Identify the blood parasite species.
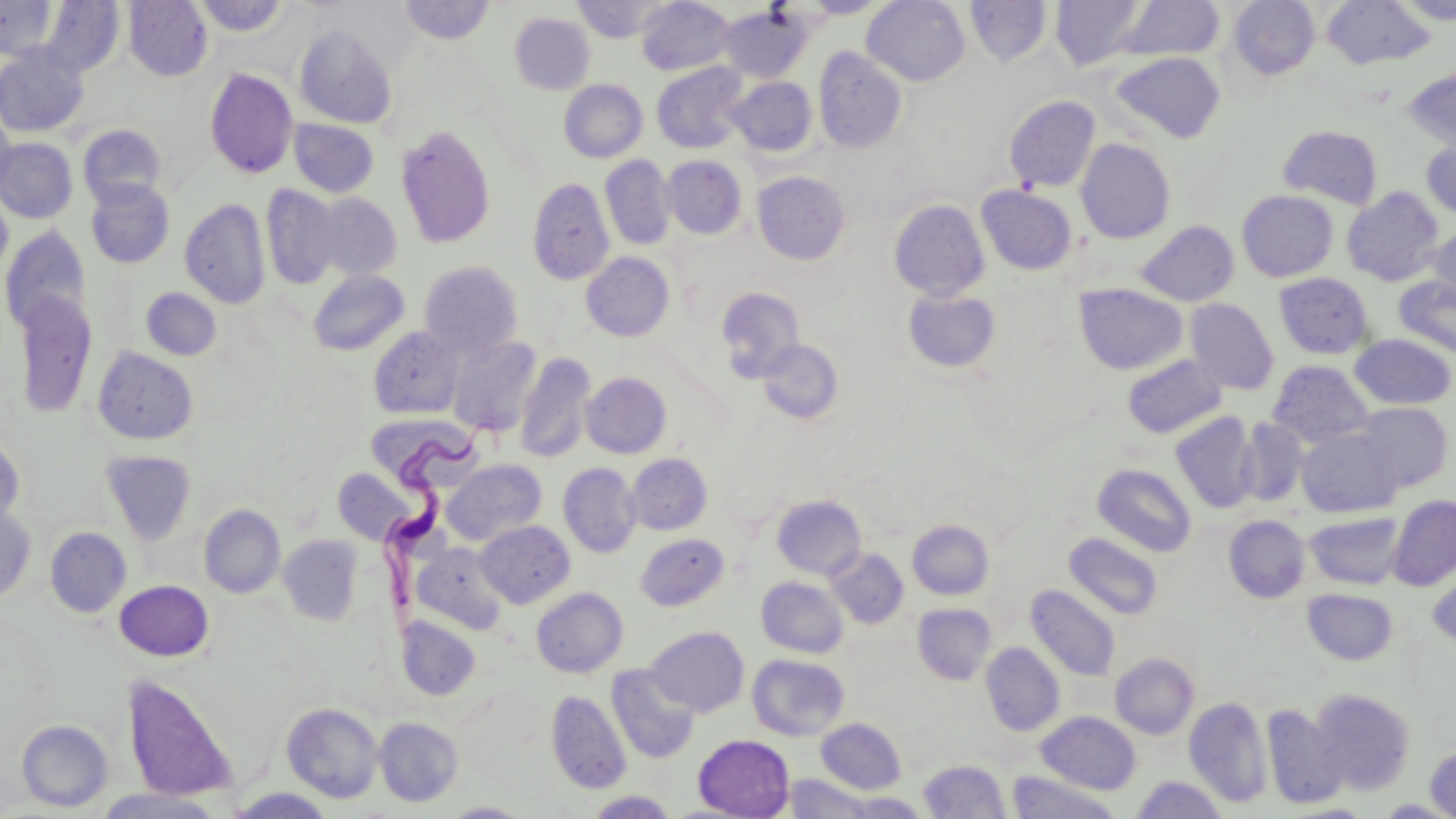

Trypanosoma brucei.

Summary:
  - Coordinate format: approximate bounding boxes as [x1, y1, x2, y2] in pixels
  - Trypanosoma brucei locations: [381, 416, 513, 619]
  - Uninfected red blood cell locations: [0, 0, 59, 60], [123, 0, 213, 81], [195, 0, 289, 37], [572, 0, 672, 42], [636, 0, 736, 76], [802, 0, 888, 18], [862, 0, 971, 86], [1049, 0, 1150, 71], [1228, 0, 1320, 80], [1321, 0, 1436, 69], [1397, 0, 1456, 25], [39, 1, 125, 78], [398, 1, 495, 45], [966, 1, 1053, 67], [1113, 1, 1225, 62], [719, 5, 814, 84], [510, 13, 595, 95], [294, 24, 398, 129], [0, 45, 89, 138], [814, 46, 908, 153], [1110, 51, 1226, 143], [652, 62, 750, 154], [1401, 66, 1456, 152], [204, 67, 299, 179], [728, 76, 817, 157], [558, 79, 648, 163], [1004, 95, 1100, 192], [0, 113, 17, 204], [288, 118, 379, 198], [77, 124, 167, 208], [395, 124, 497, 250], [1277, 125, 1383, 209], [0, 138, 78, 223], [1421, 138, 1456, 220], [1076, 139, 1175, 244], [600, 155, 675, 250], [662, 156, 747, 239], [753, 171, 851, 264], [527, 177, 614, 286], [85, 179, 175, 269], [261, 184, 341, 290], [976, 185, 1078, 276], [1342, 187, 1444, 286], [1237, 190, 1339, 282], [0, 192, 13, 279], [310, 192, 402, 280], [180, 198, 271, 309], [889, 199, 990, 301], [1136, 220, 1239, 306], [0, 225, 91, 336], [1429, 225, 1456, 307], [581, 252, 675, 341], [419, 261, 524, 356], [308, 269, 409, 356], [1274, 272, 1373, 359], [1394, 276, 1456, 359], [1074, 283, 1188, 375], [140, 287, 222, 360], [716, 287, 804, 382], [902, 288, 1001, 373], [14, 291, 97, 419], [1185, 298, 1279, 395], [368, 326, 465, 419], [1350, 333, 1455, 410], [447, 336, 543, 437], [757, 338, 844, 425], [92, 346, 199, 445], [515, 353, 596, 463], [1122, 354, 1227, 438], [1267, 360, 1374, 448], [581, 372, 672, 458], [1354, 402, 1453, 492], [1171, 412, 1259, 513], [1236, 418, 1310, 508], [369, 420, 481, 490], [1297, 427, 1404, 517], [0, 438, 25, 531], [101, 450, 198, 545], [627, 453, 712, 535], [442, 459, 546, 546], [558, 462, 642, 558], [1092, 463, 1197, 556], [332, 467, 416, 545], [1387, 494, 1456, 590], [771, 495, 867, 580], [0, 503, 36, 604], [199, 504, 285, 598], [1305, 512, 1405, 590], [1224, 515, 1311, 603], [476, 520, 574, 608], [907, 520, 994, 600], [45, 527, 131, 617], [1065, 532, 1163, 620], [636, 534, 729, 611], [278, 535, 363, 626], [414, 543, 508, 635], [825, 548, 909, 629], [1427, 566, 1456, 651], [756, 576, 849, 658], [114, 580, 214, 661], [1026, 584, 1121, 681], [532, 588, 628, 677], [1302, 588, 1398, 666], [912, 603, 996, 685], [396, 616, 481, 701], [646, 627, 749, 717], [981, 642, 1064, 736], [1111, 653, 1199, 739], [747, 654, 849, 740], [607, 664, 699, 764], [121, 672, 239, 803], [1310, 688, 1417, 795], [546, 689, 630, 794], [1184, 697, 1272, 807], [282, 702, 383, 803], [1261, 704, 1347, 809], [1037, 711, 1141, 794], [374, 716, 463, 807], [816, 718, 906, 794], [16, 720, 113, 811], [693, 734, 794, 818], [1425, 743, 1456, 819], [918, 760, 1010, 818], [1007, 770, 1120, 818], [782, 773, 878, 818], [1132, 776, 1228, 819], [89, 787, 226, 819], [225, 788, 337, 818], [587, 790, 678, 818], [839, 792, 931, 818], [1378, 799, 1452, 818], [442, 802, 533, 817]
  - Field of view: one of a larger specimen
  - Modality: light microscopy
  - Preparation: thin blood smear
  - Magnification: 1000x
  - Image size: 1456×819 pixels
  - Stain: May-Grünwald-Giemsa